Identify the parasite.
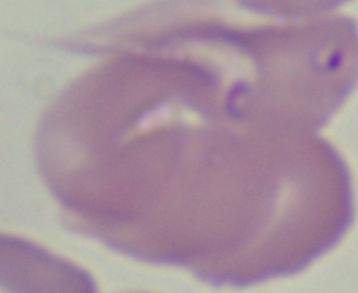
Babesia.

Summary:
  - Modality: photomicrograph
  - Magnification: 1000x